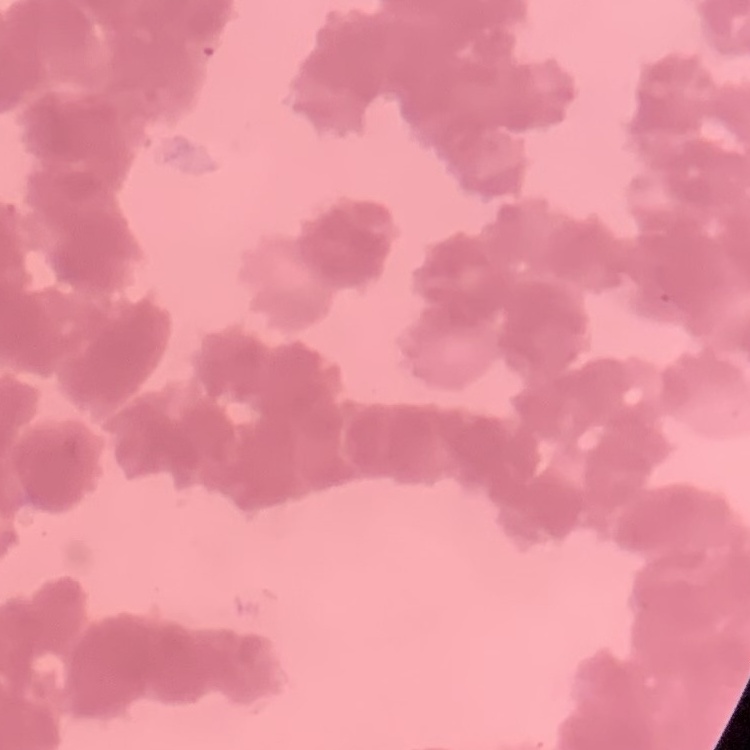

The erythrocytes show rouleaux formation. Square crop of a larger photomicrograph. Stained with either Field's or Giemsa. Thin peripheral smear.